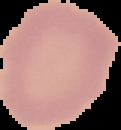
result = no Plasmodium parasites seen
image size = 121×130 pixels
image type = cell region segmented out of the field of view; surrounding area masked to black
preparation = thin blood smear